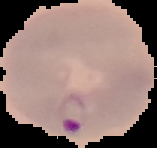

Summary:
  - Image type: cell region segmented out of the field of view; surrounding area masked to black
  - Preparation: thin blood smear
  - Image size: 157×148 pixels
  - Malaria status: parasitized